Point out each Plasmodium parasite.
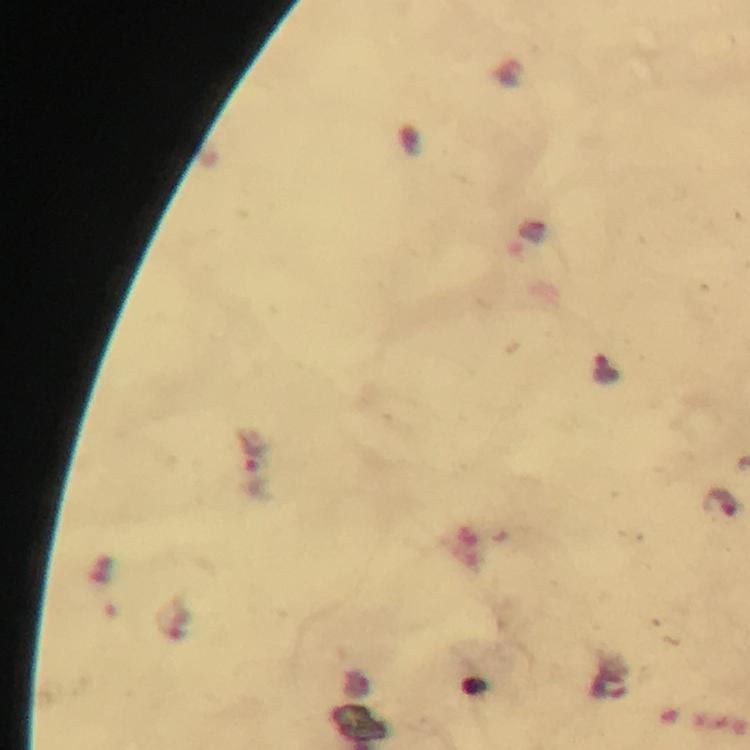
Approximate centers as {x, y} in pixels.
Plasmodium parasites: {606, 371}, {252, 466}, {720, 503}.

Summary:
  - Stain: Giemsa
  - Capture: smartphone mounted on the microscope
  - Cropped from: one field of view
  - Immersion oil: applied
  - Image size: 750×750 pixels
  - Preparation: thick blood smear
  - Context: from a malaria diagnostic workup
  - Magnification: 100x